Assess this cell for malaria.
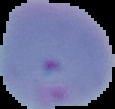

It is parasitized.

preparation = thin blood smear
image type = segmented cell region with the area outside set to black
image size = 115×109 pixels